Name the cell type shown.
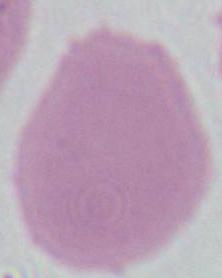

An erythrocyte.

Photomicrograph. 1000x magnification.